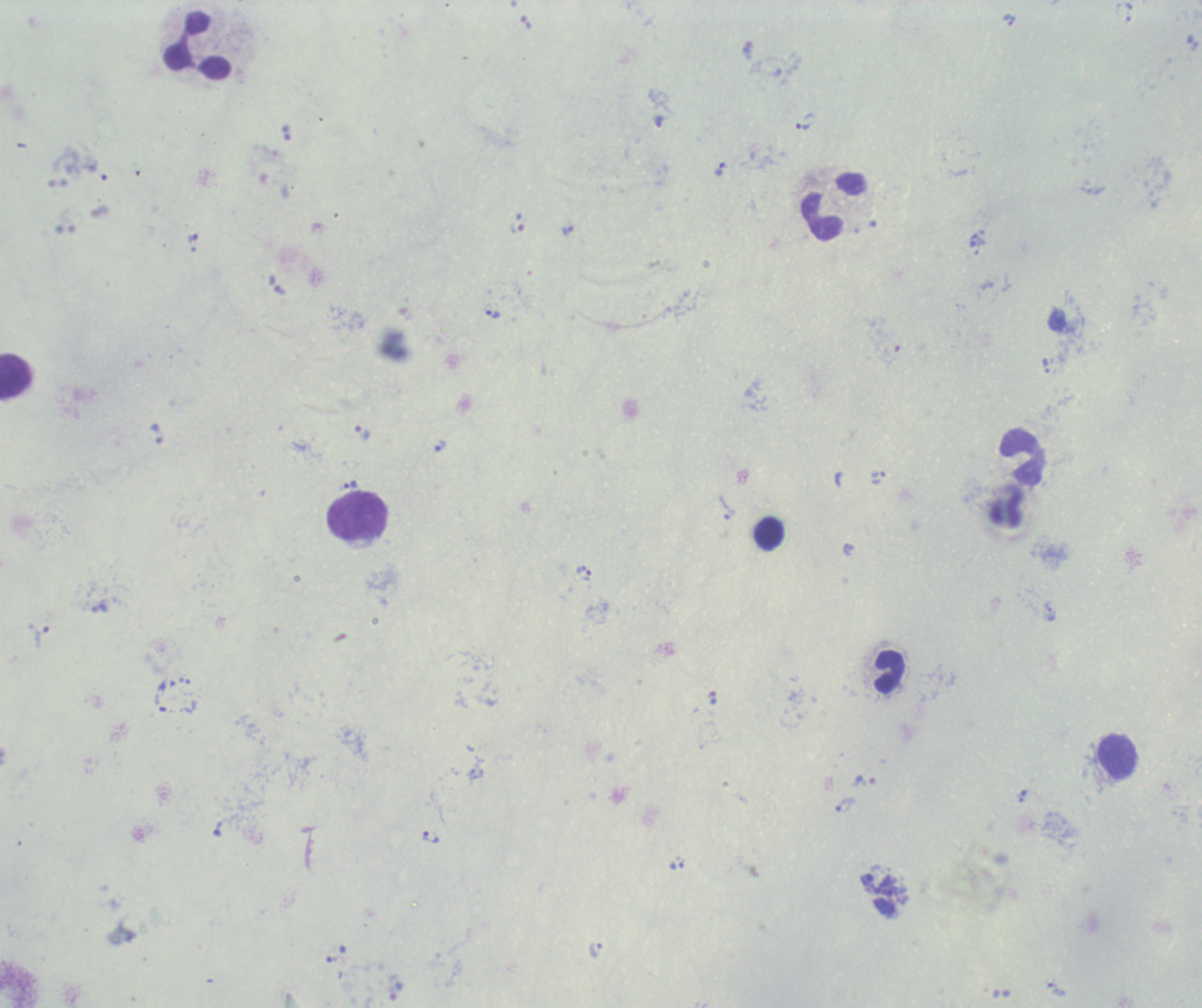 Approximate centers as [x, y] in pixels. Trophozoite locations: [1129, 12], [1009, 20], [805, 122], [719, 169], [516, 228], [567, 230], [193, 237], [493, 314], [1046, 365], [362, 433], [441, 445], [878, 477], [352, 485], [726, 507], [849, 549], [583, 572], [99, 606], [1049, 611], [38, 636], [160, 703], [863, 781], [1022, 796], [845, 805], [431, 837], [677, 863], [595, 950], [1056, 989]. Leukocyte locations: [197, 46], [832, 206], [15, 376], [1022, 456], [358, 517], [769, 533], [890, 673], [1117, 757]. Single field of view. Thick blood smear. Result: malaria parasites identified. Captured at 100x magnification. Background quality: unsatisfactory. Image is 1202×1008 pixels. Previously used in an actual diagnosis. Romanowsky-stained preparation.